Point out each leukocyte.
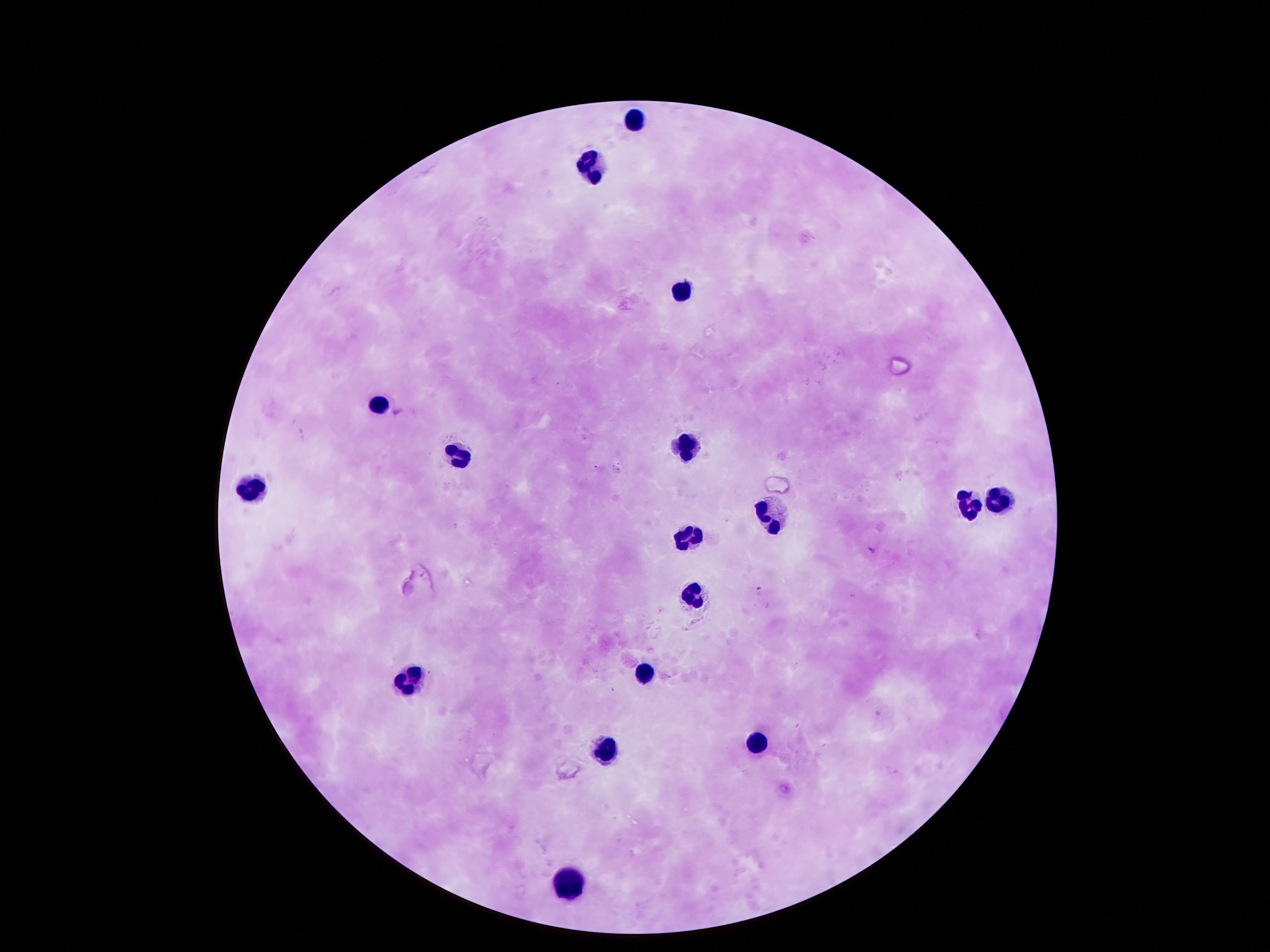

Approximate centers as {x, y} in pixels.
Leukocytes: {635, 122}, {592, 167}, {679, 288}, {380, 401}, {682, 442}, {457, 456}, {249, 493}, {998, 500}, {968, 505}, {766, 516}, {689, 535}, {693, 594}, {645, 673}, {413, 678}, {753, 744}, {605, 745}, {568, 881}.

preparation = thick blood smear
patient malaria status = uninfected
stain = Giemsa
capture = smartphone camera through the microscope eyepiece
field of view = one from this slide
image size = 1270×952 pixels
magnification = 100x